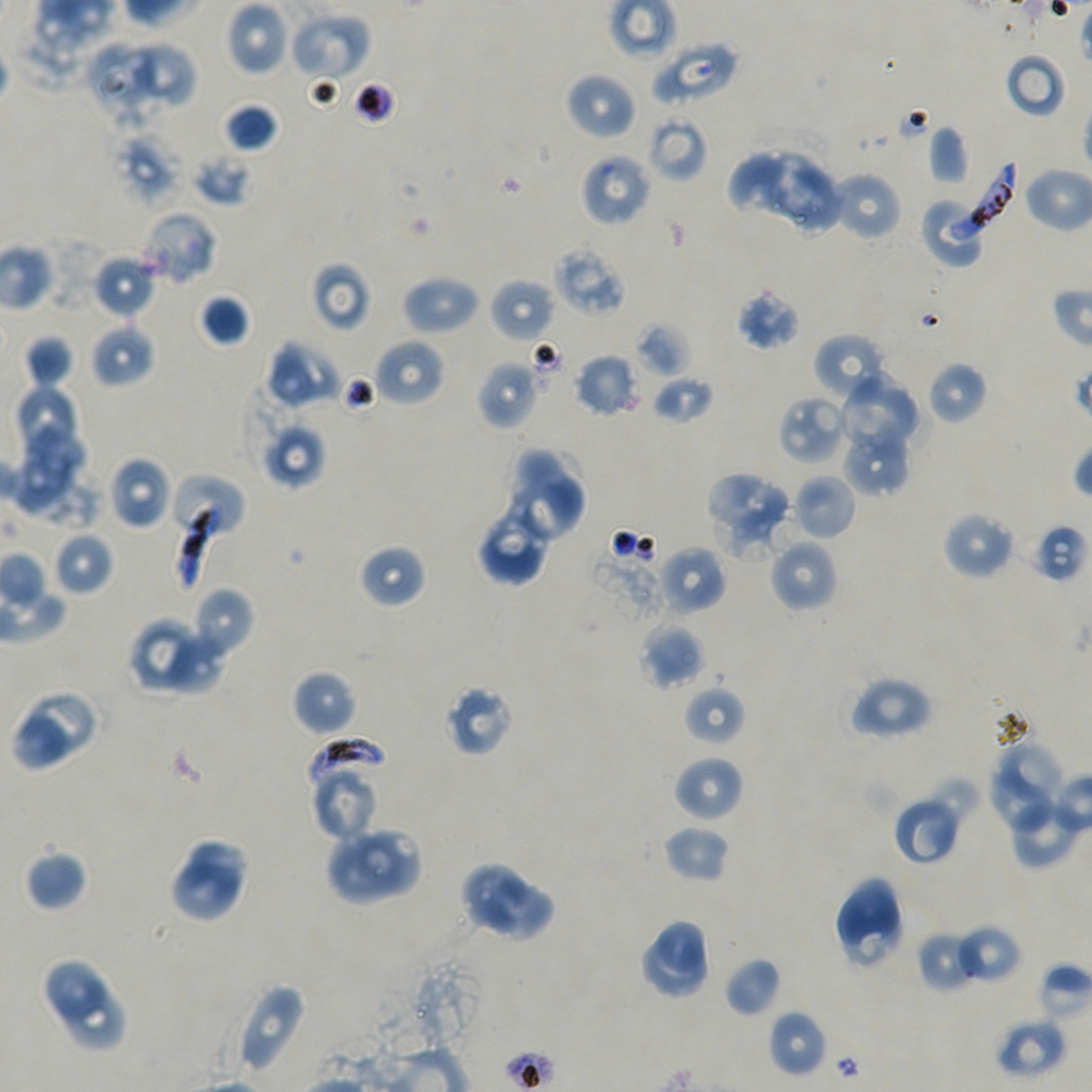 Approximate bounding boxes as {x1, y1, x2, y2} in pixels. Not every red blood cell is marked. Locations of uninfected red blood cells: {225, 1, 289, 76}, {289, 12, 371, 81}, {88, 39, 154, 111}, {129, 39, 194, 113}, {650, 40, 740, 108}, {1004, 52, 1068, 120}, {564, 71, 637, 141}, {223, 102, 278, 152}, {647, 113, 707, 182}, {928, 125, 970, 185}, {728, 148, 840, 234}, {193, 153, 252, 206}, {829, 171, 903, 242}, {139, 211, 217, 285}, {553, 244, 627, 316}, {93, 255, 156, 319}, {310, 261, 372, 332}, {401, 274, 480, 335}, {489, 277, 556, 342}, {735, 287, 801, 351}, {198, 293, 251, 347}, {634, 321, 692, 379}, {90, 322, 156, 388}, {812, 333, 889, 401}, {24, 334, 75, 388}, {373, 338, 445, 407}, {266, 339, 342, 410}, {573, 353, 640, 417}, {476, 360, 541, 431}, {927, 361, 987, 424}, {837, 374, 920, 452}, {651, 375, 715, 424}, {14, 382, 80, 459}, {778, 395, 849, 465}, {10, 418, 86, 510}, {259, 418, 328, 490}, {841, 422, 911, 496}, {514, 445, 564, 502}, {108, 456, 174, 530}, {706, 472, 795, 556}, {505, 473, 587, 543}, {792, 474, 857, 541}, {478, 507, 549, 589}, {941, 511, 1015, 579}, {1027, 521, 1090, 583}, {52, 531, 113, 596}, {768, 537, 839, 613}, {359, 544, 426, 608}, {655, 545, 727, 617}, {189, 587, 254, 661}, {128, 617, 197, 689}, {638, 623, 706, 690}, {164, 634, 225, 693}, {292, 670, 357, 735}, {848, 675, 934, 740}, {443, 684, 514, 757}, {684, 685, 746, 746}, {26, 688, 95, 754}, {12, 715, 67, 770}, {997, 743, 1066, 799}, {672, 754, 744, 823}, {986, 769, 1053, 832}, {315, 773, 374, 841}, {927, 774, 983, 829}, {892, 795, 963, 865}, {1006, 797, 1080, 870}, {663, 824, 730, 883}, {351, 829, 423, 901}, {325, 830, 400, 905}, {188, 839, 249, 896}, {24, 850, 88, 911}, {458, 860, 527, 931}, {173, 861, 240, 923}, {833, 876, 906, 972}, {481, 879, 553, 943}, {655, 919, 706, 972}, {955, 924, 1022, 985}, {916, 930, 980, 993}, {637, 934, 707, 1002}, {723, 956, 783, 1018}, {39, 957, 106, 1027}, {1038, 962, 1092, 1025}, {236, 981, 308, 1076}, {63, 985, 126, 1053}, {768, 1010, 827, 1076}, {993, 1017, 1068, 1079}. Locations of infected red blood cells: {951, 161, 1019, 244}, {170, 498, 228, 591}, {304, 737, 389, 799}. Locations of red blood cells of indeterminate infection status: {112, 126, 185, 206}, {579, 153, 651, 228}, {920, 196, 987, 269}, {169, 473, 246, 545}. Giemsa stain. Image is 1092×1092 pixels. Single field of view. Thin blood film. 100x objective under oil immersion, numerical aperture 1.45. Plasmodium falciparum strain NF54 in static in-vitro culture. Donor blood group A+/O+.